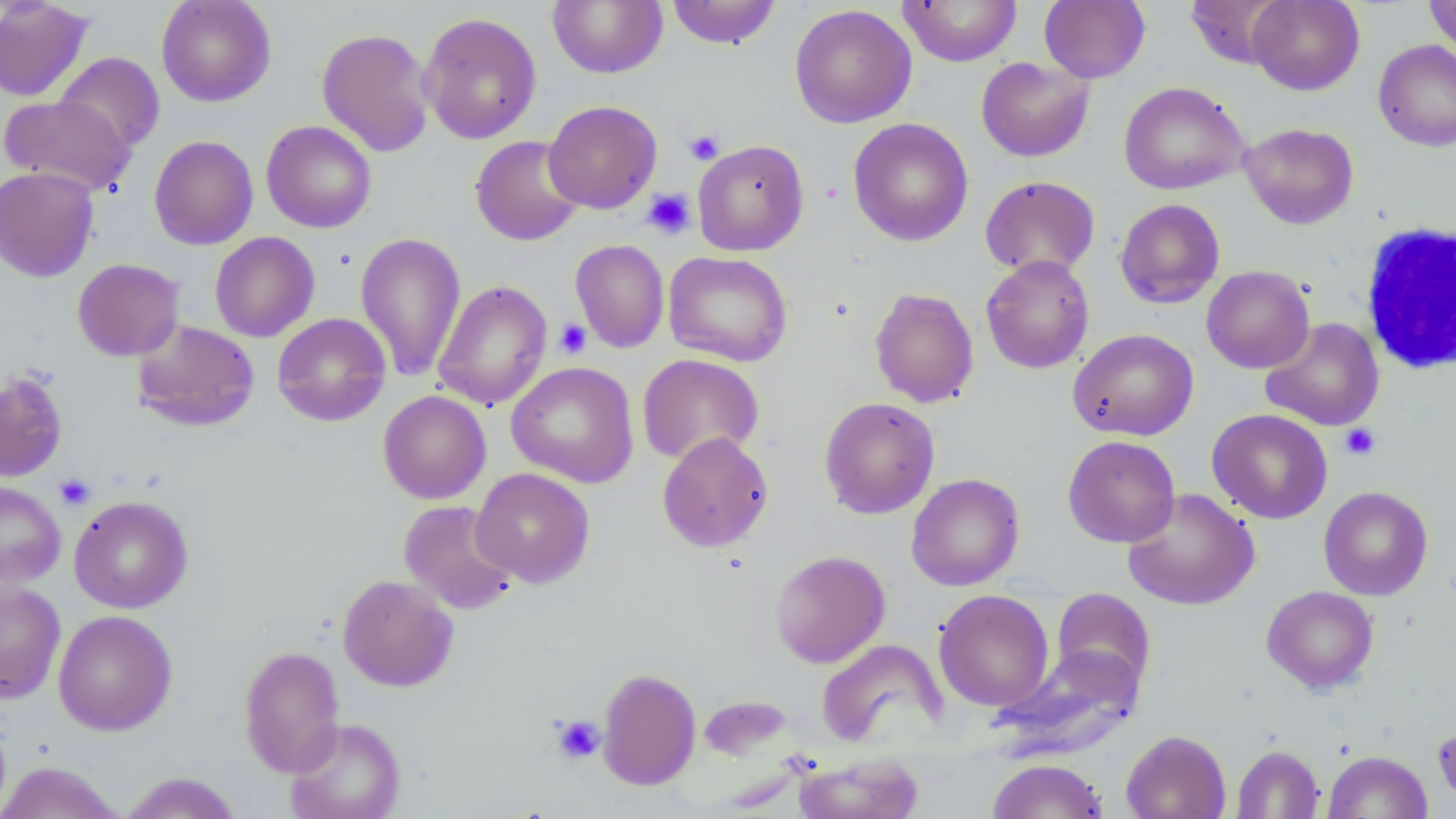 Approximate bounding boxes as named x1/y1/x2/y2 corners in pixels. White blood cell locations: (x1=1358, y1=221, x2=1454, y2=375). Uninfected red blood cell locations: (x1=0, y1=0, x2=94, y2=102), (x1=156, y1=0, x2=276, y2=107), (x1=548, y1=0, x2=668, y2=78), (x1=666, y1=0, x2=781, y2=49), (x1=898, y1=0, x2=1022, y2=66), (x1=1039, y1=0, x2=1151, y2=83), (x1=1186, y1=0, x2=1291, y2=69), (x1=1247, y1=0, x2=1364, y2=95), (x1=1424, y1=0, x2=1456, y2=58), (x1=789, y1=3, x2=917, y2=129), (x1=419, y1=11, x2=542, y2=144), (x1=316, y1=27, x2=435, y2=157), (x1=1373, y1=40, x2=1456, y2=152), (x1=53, y1=51, x2=165, y2=153), (x1=976, y1=57, x2=1094, y2=162), (x1=1119, y1=81, x2=1250, y2=195), (x1=0, y1=94, x2=135, y2=196), (x1=543, y1=100, x2=662, y2=213), (x1=848, y1=118, x2=974, y2=246), (x1=261, y1=120, x2=377, y2=233), (x1=1240, y1=122, x2=1358, y2=229), (x1=149, y1=135, x2=259, y2=250), (x1=470, y1=135, x2=586, y2=246), (x1=692, y1=139, x2=809, y2=256), (x1=1, y1=166, x2=100, y2=283), (x1=980, y1=175, x2=1100, y2=278), (x1=1114, y1=198, x2=1225, y2=309), (x1=209, y1=232, x2=320, y2=342), (x1=355, y1=232, x2=467, y2=381), (x1=570, y1=239, x2=669, y2=353), (x1=664, y1=250, x2=793, y2=367), (x1=981, y1=254, x2=1094, y2=374), (x1=72, y1=258, x2=184, y2=361), (x1=1201, y1=265, x2=1315, y2=374), (x1=433, y1=280, x2=553, y2=410), (x1=869, y1=287, x2=979, y2=407), (x1=272, y1=313, x2=391, y2=426), (x1=1261, y1=317, x2=1384, y2=431), (x1=131, y1=319, x2=260, y2=432), (x1=1068, y1=328, x2=1198, y2=441), (x1=637, y1=353, x2=764, y2=465), (x1=507, y1=361, x2=639, y2=487), (x1=0, y1=371, x2=68, y2=481), (x1=378, y1=390, x2=491, y2=504), (x1=819, y1=396, x2=940, y2=519), (x1=1207, y1=409, x2=1333, y2=524), (x1=657, y1=431, x2=774, y2=552), (x1=1062, y1=435, x2=1181, y2=548), (x1=471, y1=468, x2=595, y2=587), (x1=906, y1=472, x2=1025, y2=591), (x1=0, y1=480, x2=66, y2=589), (x1=1319, y1=486, x2=1433, y2=600), (x1=1122, y1=487, x2=1260, y2=610), (x1=69, y1=495, x2=193, y2=614), (x1=398, y1=500, x2=520, y2=615), (x1=769, y1=549, x2=890, y2=668), (x1=338, y1=574, x2=458, y2=692), (x1=0, y1=580, x2=66, y2=704), (x1=1262, y1=585, x2=1379, y2=693), (x1=1050, y1=587, x2=1157, y2=695), (x1=934, y1=588, x2=1054, y2=711), (x1=53, y1=610, x2=178, y2=735), (x1=816, y1=638, x2=946, y2=748), (x1=238, y1=645, x2=345, y2=777), (x1=992, y1=648, x2=1143, y2=759), (x1=597, y1=667, x2=701, y2=790), (x1=698, y1=695, x2=795, y2=762), (x1=285, y1=717, x2=406, y2=819), (x1=1433, y1=721, x2=1456, y2=810), (x1=1120, y1=729, x2=1231, y2=819), (x1=1231, y1=744, x2=1324, y2=818), (x1=1323, y1=750, x2=1433, y2=818), (x1=792, y1=754, x2=925, y2=819), (x1=987, y1=758, x2=1109, y2=819), (x1=0, y1=761, x2=125, y2=819), (x1=118, y1=771, x2=244, y2=818). Platelet locations: (x1=685, y1=130, x2=724, y2=165), (x1=643, y1=188, x2=695, y2=239), (x1=554, y1=319, x2=592, y2=359), (x1=1340, y1=424, x2=1380, y2=460), (x1=55, y1=474, x2=96, y2=510), (x1=551, y1=715, x2=605, y2=764). Slide-level diagnosis: negative for blood parasites. 1000x magnification. Thin blood smear. One field of a larger specimen. Light microscopy. Image is 1456×819 pixels. May-Grünwald-Giemsa stain.